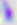
Summary:
  - Magnification: 400x
  - Identification: Toxoplasma gondii
  - Modality: micrograph